Report the malaria status of this cell.
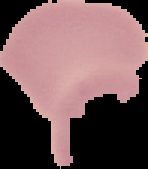
Uninfected.

Summary:
  - Preparation: thin blood smear
  - Image type: segmented cell region with the area outside set to black
  - Image size: 148×169 pixels